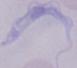
modality: micrograph
identification: trypanosome
magnification: 1000x